Locate and identify every blood parasite.
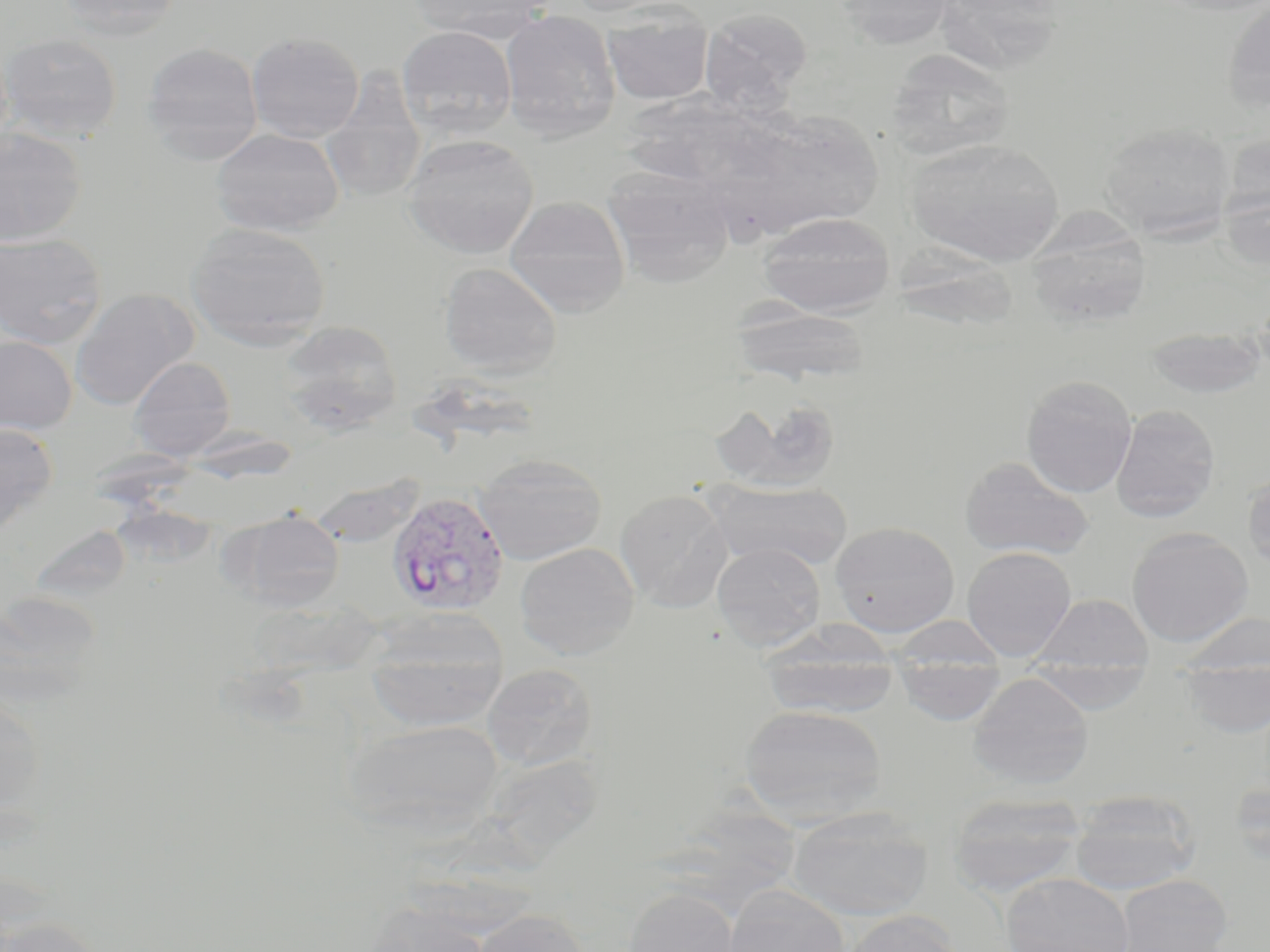

Approximate bounding boxes as named x1/y1/x2/y2 corners in pixels.
Plasmodium vivax-infected red blood cells: (x1=387, y1=491, x2=510, y2=617).
No Plasmodium falciparum, Plasmodium ovale, Plasmodium malariae, Babesia divergens, or Trypanosoma brucei observed.

Uninfected red blood cell locations: (x1=56, y1=0, x2=184, y2=40), (x1=410, y1=0, x2=553, y2=43), (x1=562, y1=0, x2=684, y2=17), (x1=834, y1=0, x2=956, y2=50), (x1=1156, y1=0, x2=1270, y2=17), (x1=1222, y1=1, x2=1270, y2=112), (x1=601, y1=5, x2=714, y2=105), (x1=700, y1=8, x2=812, y2=113), (x1=500, y1=10, x2=622, y2=141), (x1=396, y1=26, x2=518, y2=139), (x1=246, y1=31, x2=365, y2=143), (x1=0, y1=33, x2=123, y2=142), (x1=141, y1=41, x2=263, y2=163), (x1=883, y1=48, x2=1017, y2=163), (x1=320, y1=70, x2=427, y2=205), (x1=746, y1=110, x2=885, y2=234), (x1=1100, y1=122, x2=1235, y2=241), (x1=0, y1=127, x2=86, y2=246), (x1=211, y1=128, x2=344, y2=236), (x1=1220, y1=129, x2=1270, y2=219), (x1=403, y1=133, x2=538, y2=259), (x1=905, y1=138, x2=1065, y2=266), (x1=603, y1=166, x2=737, y2=287), (x1=1219, y1=183, x2=1269, y2=273), (x1=504, y1=196, x2=631, y2=318), (x1=755, y1=212, x2=896, y2=317), (x1=186, y1=221, x2=331, y2=349), (x1=1025, y1=221, x2=1153, y2=329), (x1=0, y1=232, x2=107, y2=350), (x1=899, y1=243, x2=1027, y2=338), (x1=439, y1=262, x2=562, y2=378), (x1=70, y1=288, x2=199, y2=411), (x1=729, y1=303, x2=872, y2=387), (x1=278, y1=320, x2=403, y2=434), (x1=1144, y1=327, x2=1267, y2=399), (x1=0, y1=335, x2=77, y2=434), (x1=129, y1=356, x2=236, y2=460), (x1=1020, y1=375, x2=1138, y2=498), (x1=711, y1=396, x2=843, y2=494), (x1=1111, y1=404, x2=1220, y2=523), (x1=0, y1=422, x2=58, y2=538), (x1=474, y1=454, x2=607, y2=564), (x1=959, y1=456, x2=1095, y2=561), (x1=1242, y1=471, x2=1270, y2=573), (x1=706, y1=479, x2=853, y2=572), (x1=615, y1=489, x2=733, y2=612), (x1=232, y1=511, x2=345, y2=612), (x1=830, y1=521, x2=960, y2=638), (x1=1127, y1=527, x2=1253, y2=647), (x1=514, y1=542, x2=640, y2=660), (x1=712, y1=543, x2=826, y2=651), (x1=962, y1=546, x2=1076, y2=661), (x1=0, y1=590, x2=103, y2=708), (x1=1030, y1=593, x2=1154, y2=677), (x1=1175, y1=611, x2=1270, y2=679), (x1=362, y1=634, x2=508, y2=733), (x1=760, y1=637, x2=898, y2=720), (x1=893, y1=657, x2=1006, y2=726), (x1=1027, y1=658, x2=1152, y2=714), (x1=1180, y1=659, x2=1270, y2=739), (x1=482, y1=663, x2=598, y2=770), (x1=968, y1=672, x2=1094, y2=790), (x1=0, y1=693, x2=48, y2=822), (x1=739, y1=704, x2=888, y2=826), (x1=342, y1=718, x2=506, y2=839), (x1=1229, y1=777, x2=1270, y2=866), (x1=1070, y1=790, x2=1201, y2=895), (x1=947, y1=792, x2=1087, y2=898), (x1=787, y1=806, x2=933, y2=921), (x1=1001, y1=873, x2=1133, y2=952), (x1=1115, y1=874, x2=1232, y2=952), (x1=722, y1=885, x2=850, y2=952), (x1=623, y1=886, x2=741, y2=952), (x1=359, y1=902, x2=491, y2=952), (x1=470, y1=909, x2=589, y2=952), (x1=841, y1=910, x2=962, y2=952), (x1=2, y1=917, x2=106, y2=952). Slide-level diagnosis: Plasmodium vivax. 1000x magnification. Image is 1270×952 pixels. Thin blood film. Single field of view. Optical microscopy. May-Grünwald-Giemsa stain.